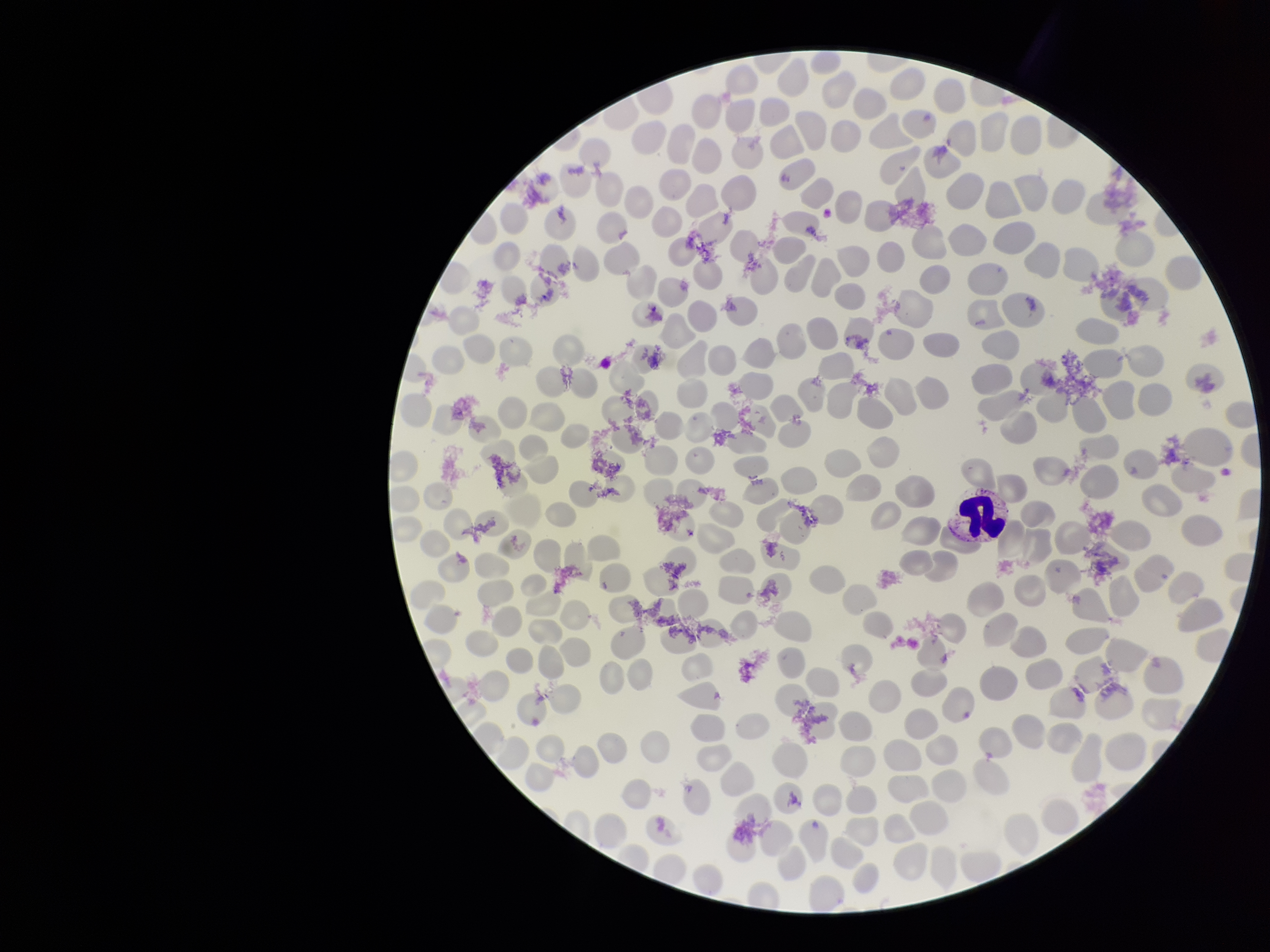
Summary:
  - Red blood cell count: 241
  - Stain: Giemsa
  - Field of view: one from this slide
  - Preparation: thin
  - Patient malaria status: negative
  - Parasitized red blood cells: none detected
  - Parasitized red blood cell count: 0
  - Image size: 1270×952 pixels
  - Capture: smartphone photograph through the microscope eyepiece